Locate every P. falciparum parasite and identify its life-cycle stage.
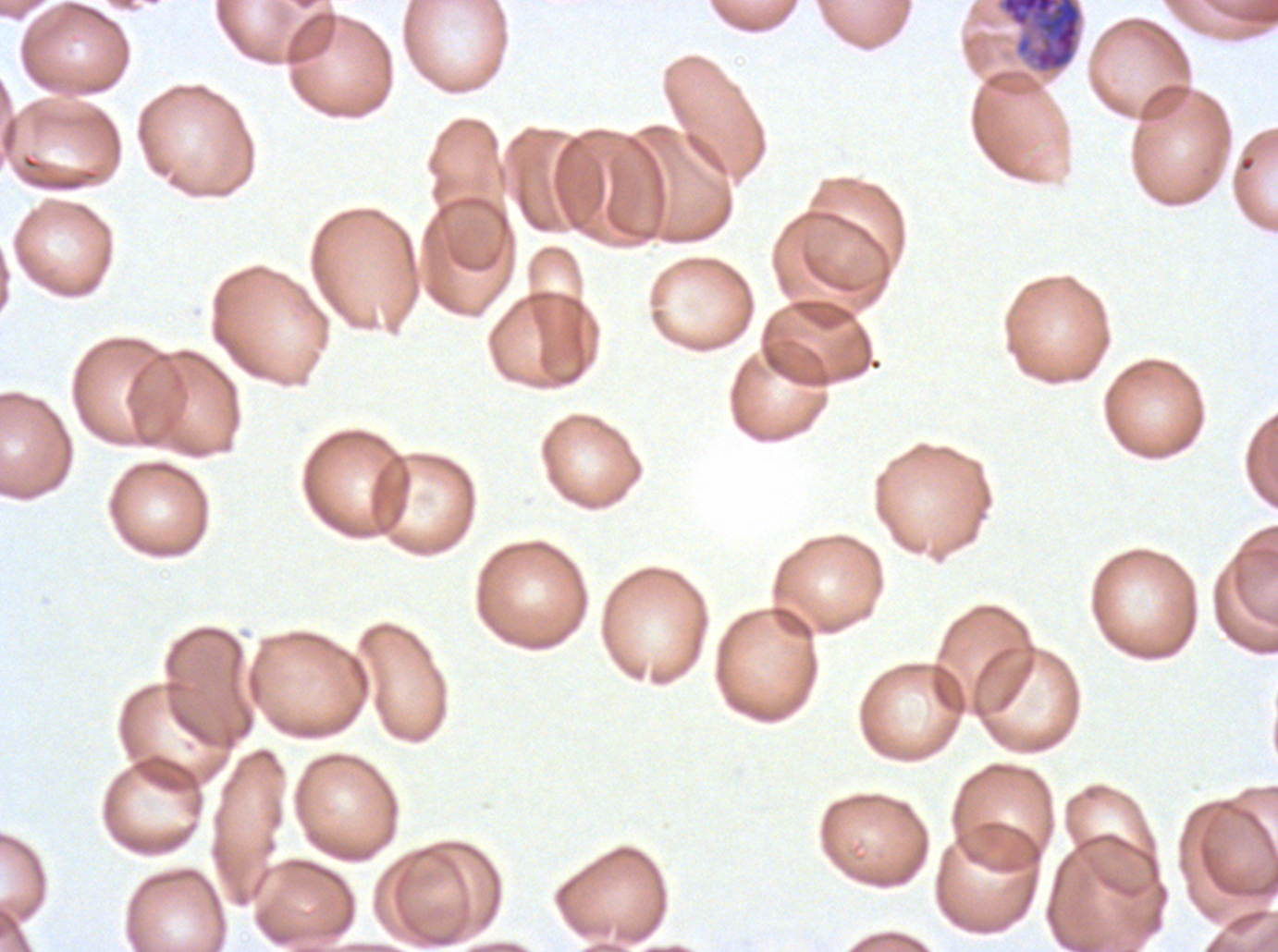
Approximate bounding rectangles given as corner coordinates in pixels from the top-left.
Late schizonts: (x1=997, y1=0, x2=1083, y2=74).
No rings, late-ring/early-trophozoite forms, mid trophozoites, late trophozoites, early schizonts, segmenters, or gametocytes observed.

P. falciparum cultured ex vivo for 24 to 48 hours, from a patient in The Gambia. Thin blood smear. Image is 1278×952 pixels. A sub-image separated from a larger composite. Giemsa stain.